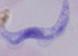

Summary:
  - Identification: trypanosome
  - Modality: micrograph
  - Magnification: 1000x